Give the extent of all Plasmodium falciparum-infected red blood cells.
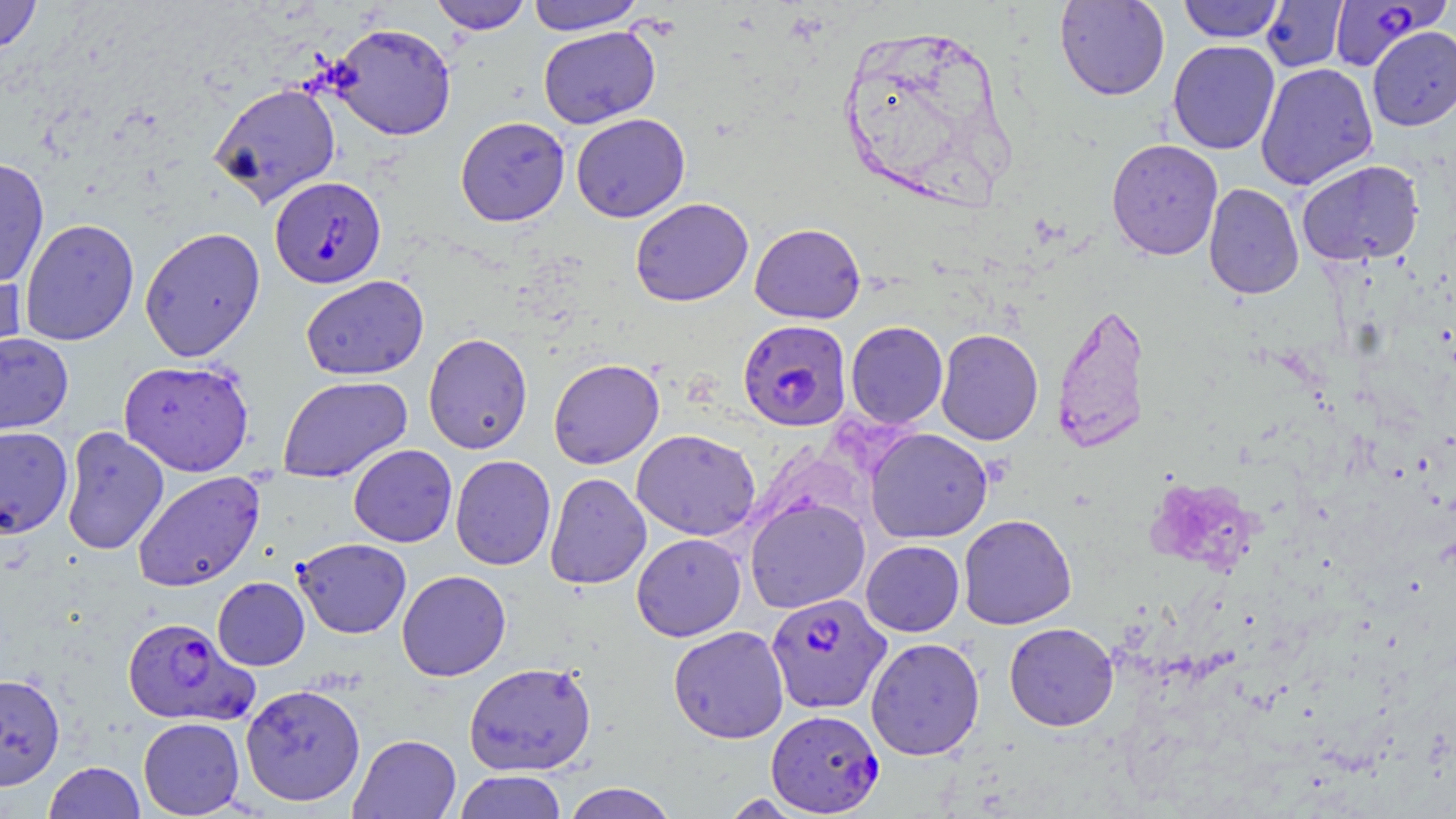
Approximate bounding boxes as (x1,y1)-(x2,y2) corner pairs in pixels.
Plasmodium falciparum-infected red blood cells: (1328,0)-(1449,71), (269,176)-(386,289), (737,319)-(852,431), (765,592)-(892,714), (121,617)-(257,727), (765,708)-(884,816).

Uninfected red blood cell locations: (0,0)-(42,54), (431,0)-(531,34), (527,0)-(645,35), (1054,0)-(1170,100), (1177,0)-(1286,42), (1260,0)-(1348,72), (328,22)-(456,140), (538,26)-(660,129), (1368,26)-(1456,130), (1167,40)-(1280,154), (1255,62)-(1379,190), (208,82)-(341,207), (571,113)-(690,222), (455,116)-(570,226), (1105,138)-(1223,260), (0,157)-(50,290), (1296,160)-(1424,266), (1203,183)-(1304,299), (630,197)-(753,306), (19,218)-(140,346), (749,223)-(866,324), (139,226)-(266,362), (0,262)-(28,378), (301,275)-(428,380), (1051,300)-(1151,455), (845,321)-(948,428), (936,328)-(1044,445), (0,332)-(74,436), (423,332)-(533,454), (119,358)-(254,477), (548,358)-(664,469), (277,375)-(413,483), (0,425)-(73,539), (60,426)-(170,556), (865,428)-(993,543), (631,429)-(761,541), (348,444)-(457,547), (450,455)-(556,570), (132,470)-(265,592), (544,472)-(651,590), (745,496)-(870,613), (958,514)-(1076,630), (631,533)-(746,641), (293,538)-(411,638), (861,540)-(964,636), (397,570)-(511,681), (212,577)-(310,671), (1004,622)-(1118,731), (668,625)-(789,743), (865,637)-(985,760), (464,662)-(597,776), (0,672)-(65,791), (240,683)-(366,807), (138,716)-(245,817), (349,734)-(461,819), (44,761)-(145,819), (454,770)-(567,818), (562,782)-(679,819). Slide-level diagnosis: Plasmodium falciparum. One field of a larger specimen. Image is 1456×819 pixels. May-Grünwald-Giemsa-stained preparation. Thin blood film. Optical microscopy. Captured at 1000x magnification.